Comment on the morphology of the erythrocytes.
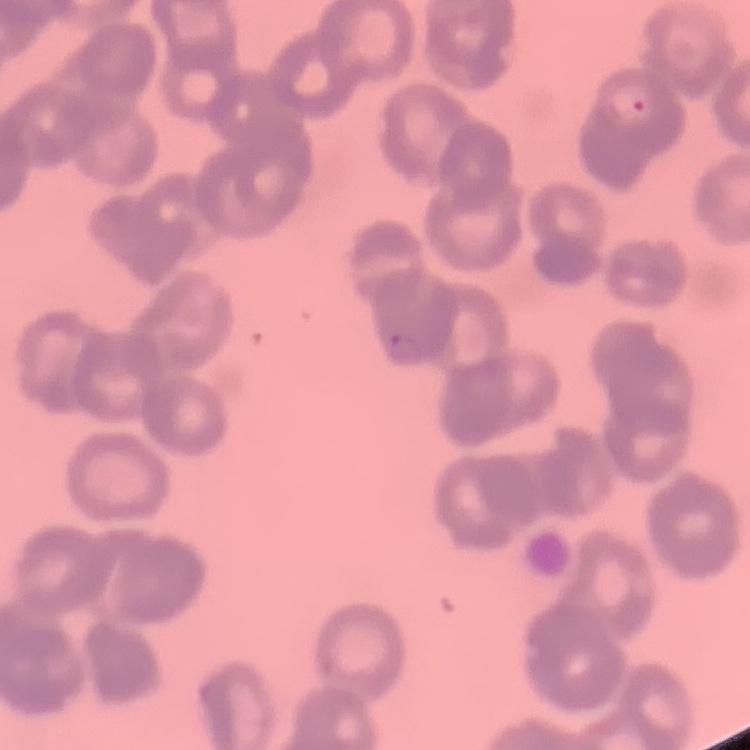
Rouleaux formation.

image type = square crop of a larger photomicrograph
stain = Field's or Giemsa
preparation = thin blood film